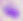

Summary:
  - Modality: micrograph
  - Magnification: 400x
  - Identification: Toxoplasma gondii